Point out each Plasmodium parasite and each leukocyte.
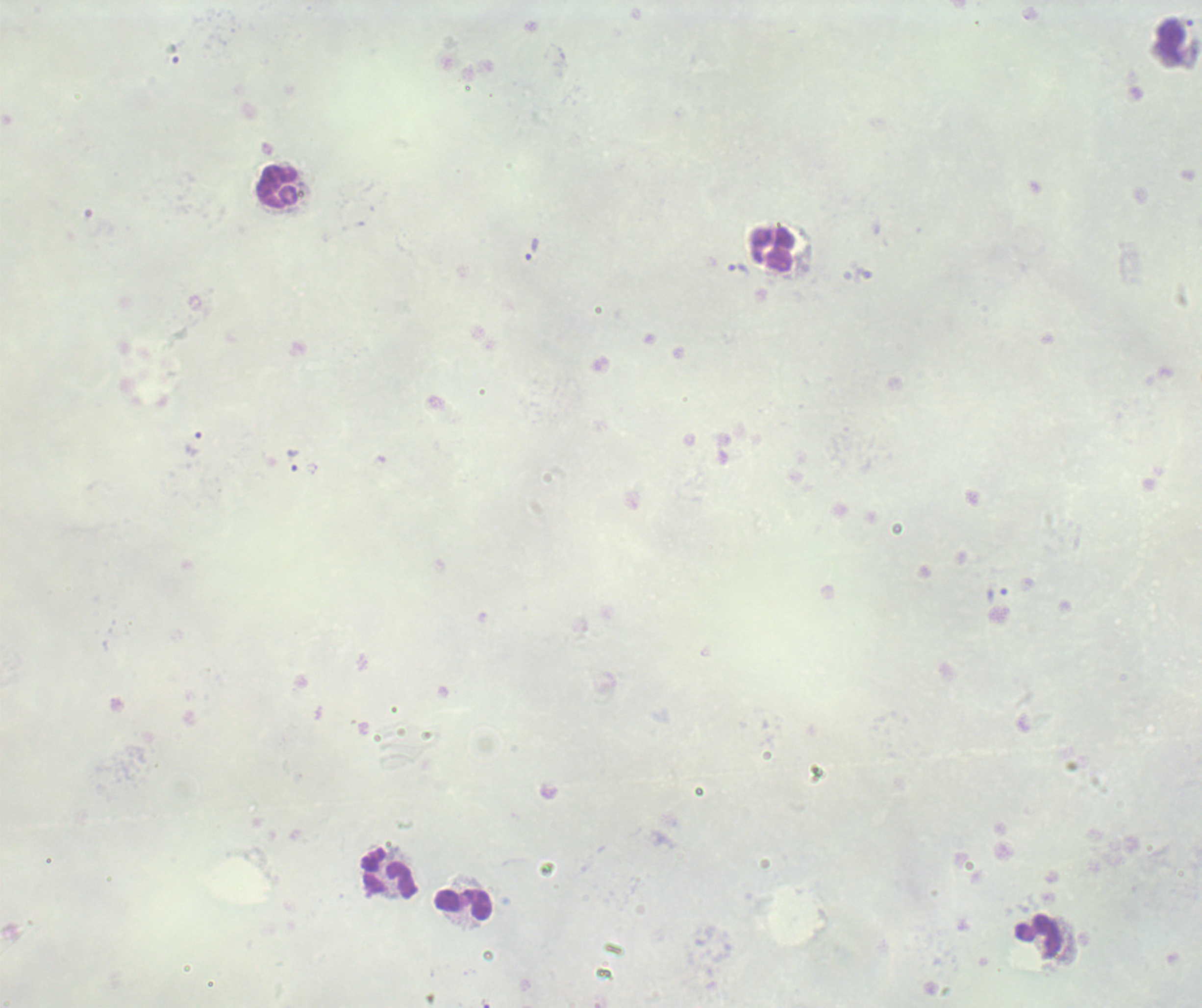

Approximate centers as (x, y) in pixels.
Trophozoites: (533, 249), (740, 269), (194, 441), (294, 461).
No schizont or gametocyte forms observed.
Leukocytes: (277, 186), (773, 249), (389, 873), (465, 904), (1039, 937).

Previously used in an actual diagnosis. Image is 1202×1008 pixels. Thick blood film. Coloration quality: bad. Background quality: unsatisfactory. Romanowsky-stained preparation. Captured at 100x magnification. Single field of view.